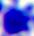

modality: photomicrograph
magnification: 400x
identification: leukocyte